Assess the morphology of the red blood cells.
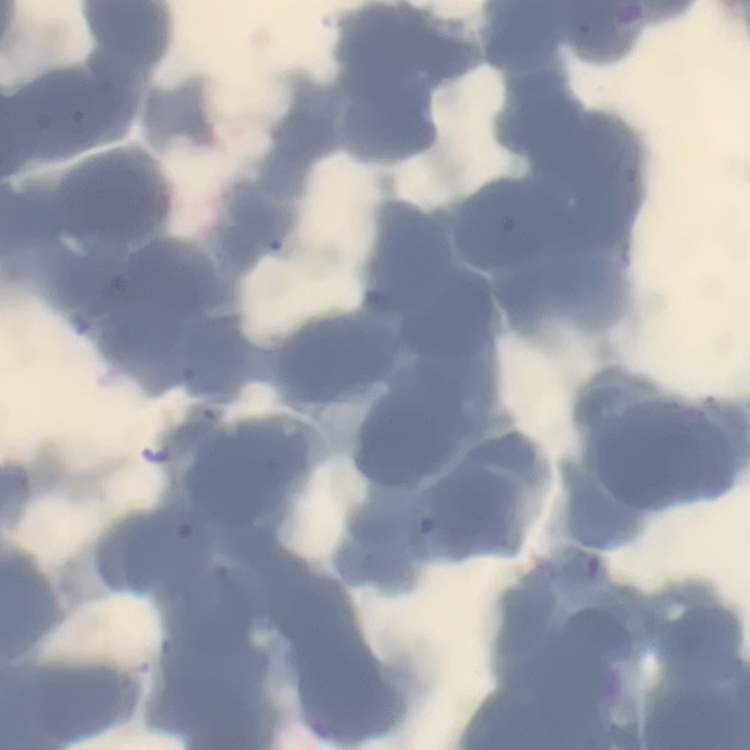
They show rouleaux formation.

Thin blood smear. Field's or Giemsa stain. Square crop of a larger photomicrograph.